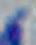 Photomicrograph. Toxoplasma gondii is shown. Captured at 1000x magnification.